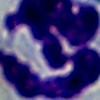
identification: white blood cell
magnification: 1000x
modality: micrograph